Report the malaria status of this cell.
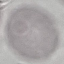
Uninfected.

{
  "capture": "smartphone camera at the microscope eyepiece",
  "image_type": "cell patch, automatically extracted from a larger field of view and resized to 64 × 64 pixels",
  "stain": "Giemsa",
  "preparation": "thin smear"
}